Evaluate for Plasmodium parasites.
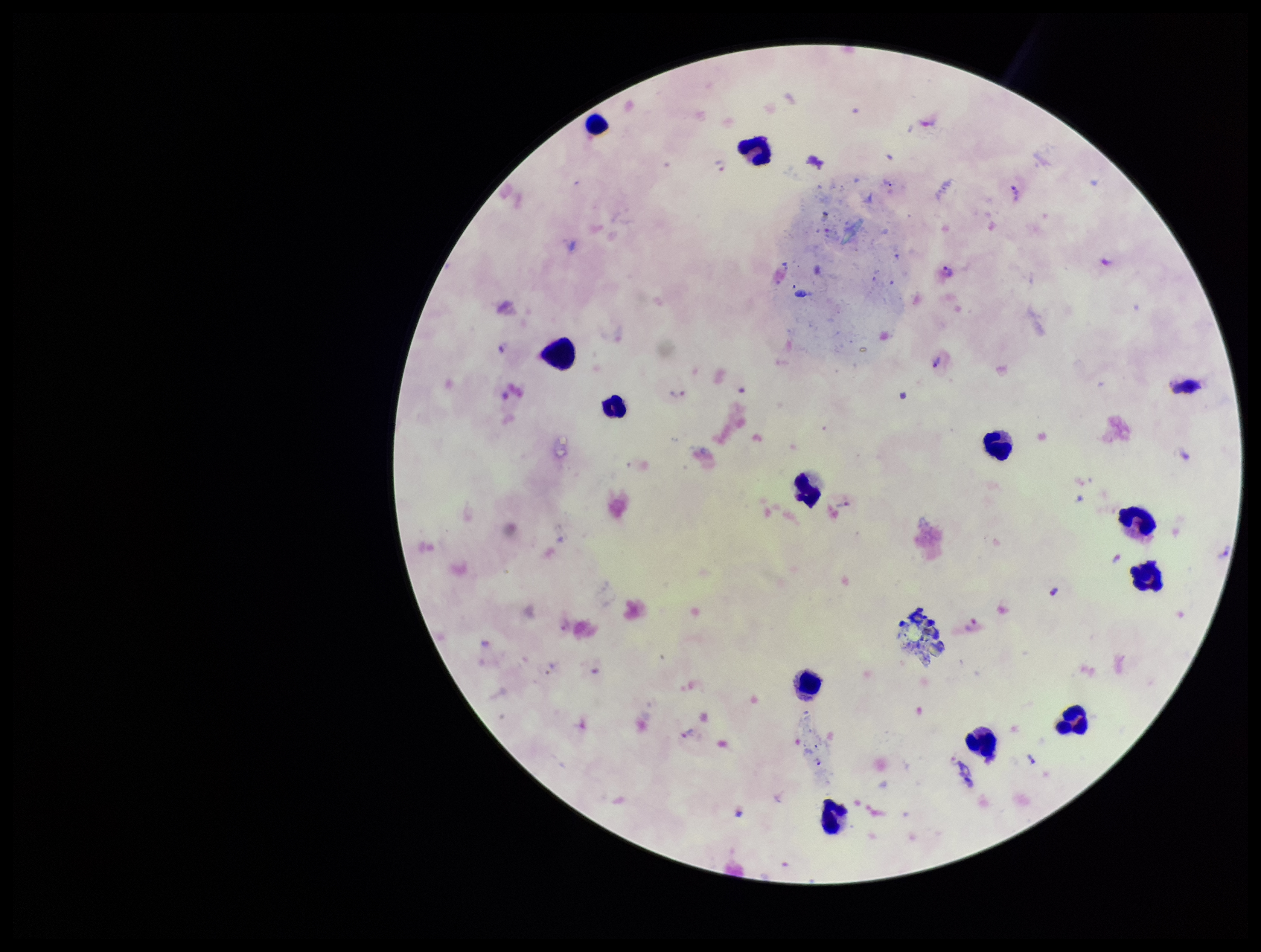

Seen.

Summary:
  - Image size: 1261×952 pixels
  - Stain: Giemsa
  - Capture: smartphone photograph through the microscope eyepiece
  - Parasite count: 6
  - Species reported for this patient: Plasmodium vivax
  - Leukocyte count: 12
  - Patient malaria status: infected
  - Preparation: thick blood smear
  - Field of view: single